Locate every parasitized red blood cell.
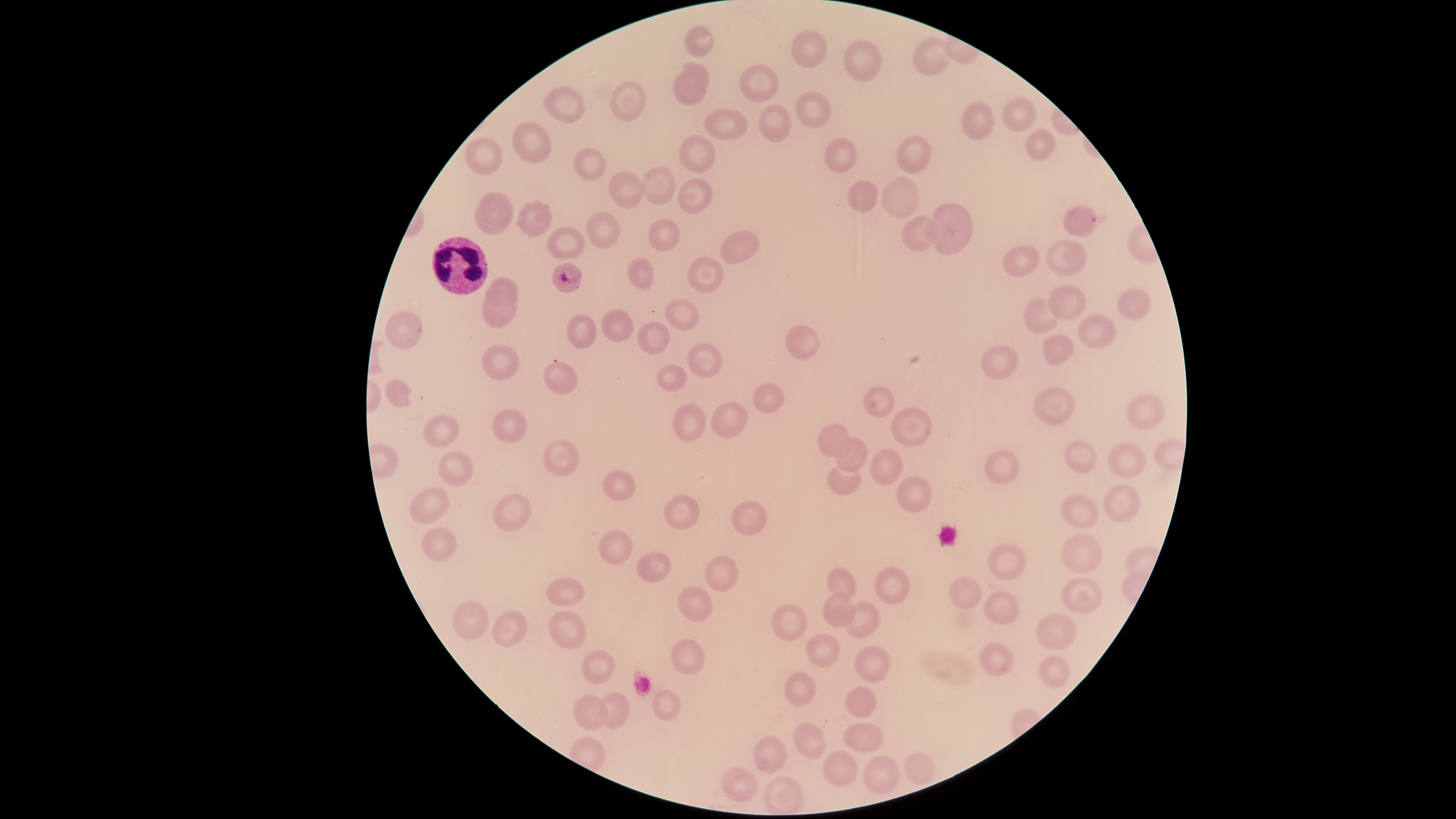
Approximate bounding boxes as [left, top, right, bottom] in pixels.
Parasitized red blood cells: [1063, 205, 1097, 237], [552, 262, 582, 292].

Approximate bounding boxes as [left, top, right, bottom] in pixels. White blood cells: [431, 236, 488, 295]. Uninfected red blood cells: [685, 25, 713, 57], [791, 28, 827, 67], [912, 37, 950, 76], [844, 39, 882, 81], [683, 62, 709, 87], [740, 64, 779, 102], [672, 70, 707, 106], [611, 81, 646, 121], [543, 86, 585, 122], [795, 91, 831, 128], [1003, 96, 1036, 132], [961, 101, 993, 141], [758, 104, 791, 142], [703, 108, 748, 140], [704, 108, 748, 139], [512, 121, 551, 165], [1025, 129, 1055, 161], [679, 134, 716, 173], [679, 135, 716, 173], [897, 136, 931, 174], [464, 137, 502, 175], [824, 138, 856, 172], [574, 147, 606, 180], [641, 166, 677, 205], [608, 171, 645, 208], [882, 176, 920, 218], [678, 177, 712, 214], [678, 178, 712, 214], [847, 180, 878, 213], [475, 191, 513, 235], [515, 199, 553, 238], [934, 203, 973, 255], [586, 211, 621, 249], [902, 216, 941, 252], [648, 218, 680, 252], [546, 225, 586, 260], [720, 230, 759, 264], [1046, 240, 1086, 276], [1002, 245, 1040, 276], [687, 256, 723, 293], [688, 256, 723, 293], [627, 257, 654, 291], [486, 277, 518, 307], [1048, 284, 1086, 320], [1117, 289, 1151, 320], [482, 294, 517, 327], [664, 298, 698, 330], [1024, 298, 1059, 334], [601, 309, 633, 342], [385, 310, 423, 349], [567, 314, 596, 349], [1078, 315, 1116, 348], [637, 321, 669, 354], [786, 325, 819, 360], [1043, 333, 1074, 367], [686, 342, 722, 377], [481, 344, 519, 382], [980, 345, 1018, 379], [543, 361, 577, 395], [657, 364, 687, 391], [385, 379, 412, 408], [753, 382, 785, 413], [864, 386, 894, 416], [1033, 386, 1075, 425], [1126, 393, 1165, 430], [711, 401, 748, 438], [673, 403, 705, 441], [891, 407, 931, 447], [492, 408, 526, 442], [424, 414, 459, 447], [817, 423, 852, 456], [836, 436, 867, 472], [542, 439, 579, 477], [1064, 440, 1097, 473], [1108, 441, 1146, 477], [870, 448, 903, 484], [438, 450, 474, 486], [985, 450, 1020, 485], [827, 464, 861, 495], [603, 470, 636, 501], [896, 475, 932, 512], [1103, 485, 1141, 522], [409, 487, 449, 524], [492, 493, 531, 531], [664, 494, 700, 530], [1060, 495, 1098, 528], [732, 501, 767, 536], [422, 527, 456, 562], [598, 529, 632, 565], [1061, 534, 1102, 573], [988, 543, 1026, 580], [636, 551, 671, 583], [705, 555, 738, 592], [827, 566, 856, 598], [875, 567, 910, 604], [949, 576, 981, 609], [546, 577, 584, 606], [1062, 577, 1103, 613], [677, 586, 712, 622], [983, 591, 1020, 625], [822, 592, 855, 628], [452, 601, 489, 640], [844, 601, 880, 639], [772, 603, 807, 641], [492, 610, 527, 647], [548, 610, 587, 649], [1036, 613, 1076, 650], [806, 633, 840, 667], [671, 639, 705, 675], [980, 642, 1013, 677], [855, 646, 891, 682], [581, 650, 615, 684], [1039, 655, 1070, 689], [785, 672, 816, 707], [846, 686, 877, 718], [652, 689, 681, 721], [599, 691, 630, 730], [573, 694, 608, 731], [794, 722, 825, 759], [844, 722, 884, 753], [754, 736, 786, 773], [823, 751, 857, 787], [905, 752, 934, 785], [863, 755, 901, 795], [722, 766, 757, 801], [764, 776, 803, 814]. Circular visible region. Thin blood film. Species: Plasmodium falciparum. Single field of view. Giemsa stain. Smartphone photograph through the microscope eyepiece. Image is 1456×819 pixels.